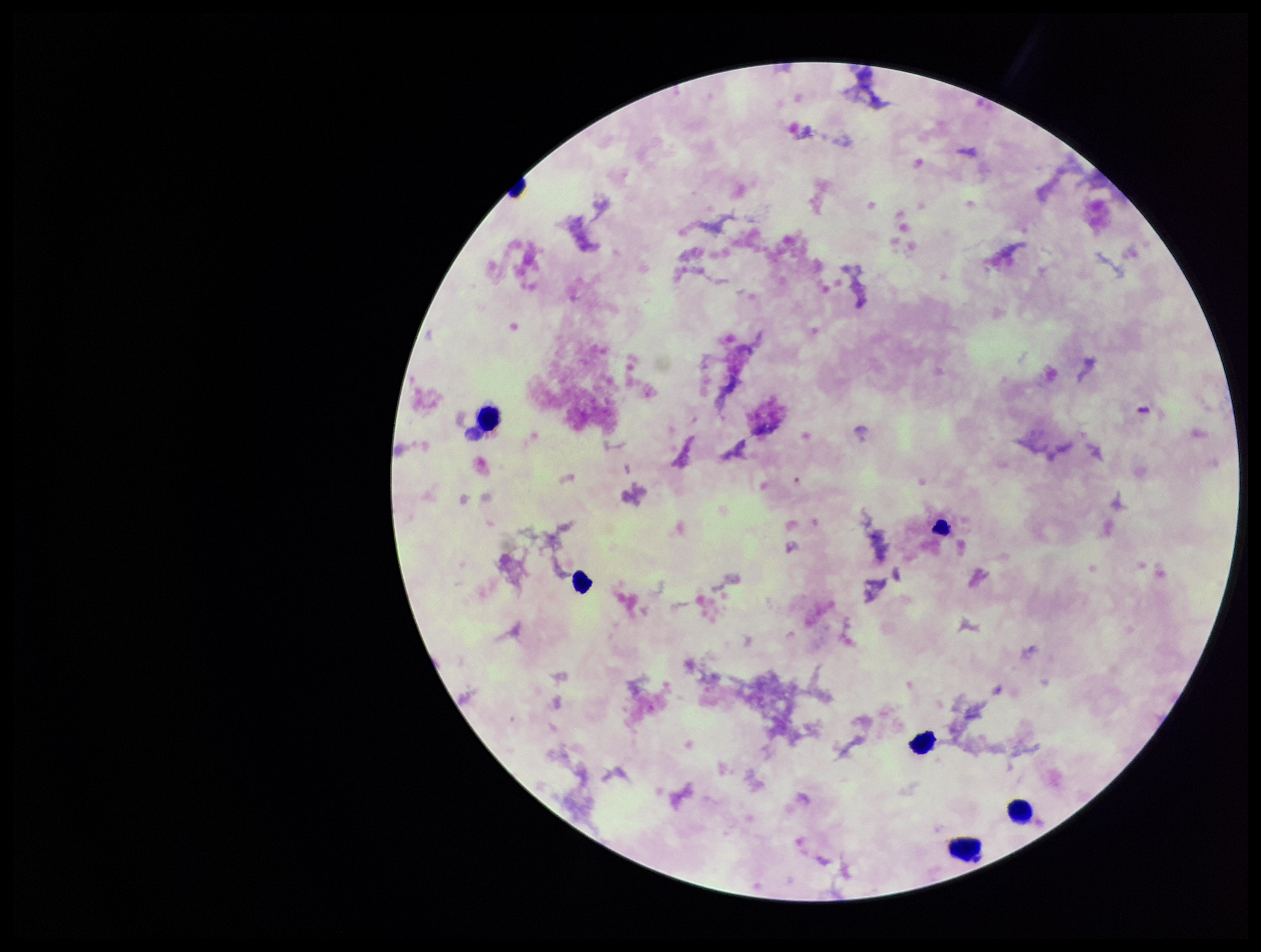

parasite_count: 0
image_size: 1261×952 pixels
capture: smartphone photograph through the microscope eyepiece
leukocyte_count: 6
plasmodium_parasites: none detected
patient_malaria_status: negative
preparation: thick blood smear
field_of_view: single
stain: Giemsa